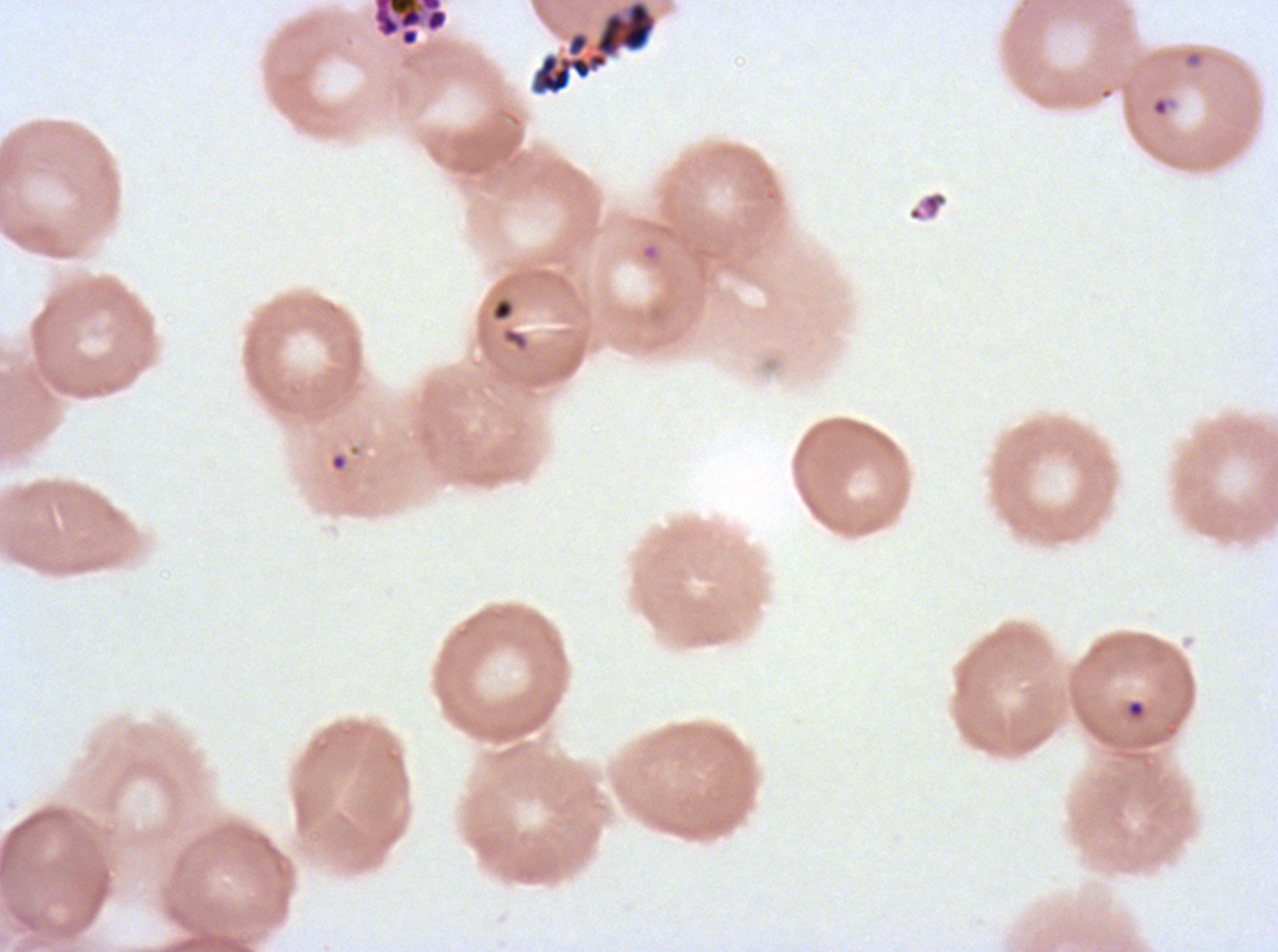
Approximate bounding rectangles given as corner coordinates in pixels from the top-left. Segmenter locations: (x1=372, y1=0, x2=449, y2=47). Debris locations: (x1=907, y1=190, x2=948, y2=222), (x1=490, y1=297, x2=515, y2=323). Ring locations: (x1=1149, y1=95, x2=1171, y2=118), (x1=1126, y1=699, x2=1146, y2=718). Image is 1278×952 pixels. Plasmodium falciparum cultured ex vivo for 24 to 48 hours, from a patient in The Gambia. Life-cycle stages observed: ring, segmenter. Giemsa-stained preparation. A sub-image separated from a larger composite. Thin blood smear.